Assess this cell for malaria.
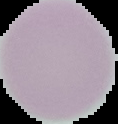

Uninfected.

Summary:
  - Image size: 118×124 pixels
  - Preparation: thin blood film
  - Image type: segmented cell region on a black background